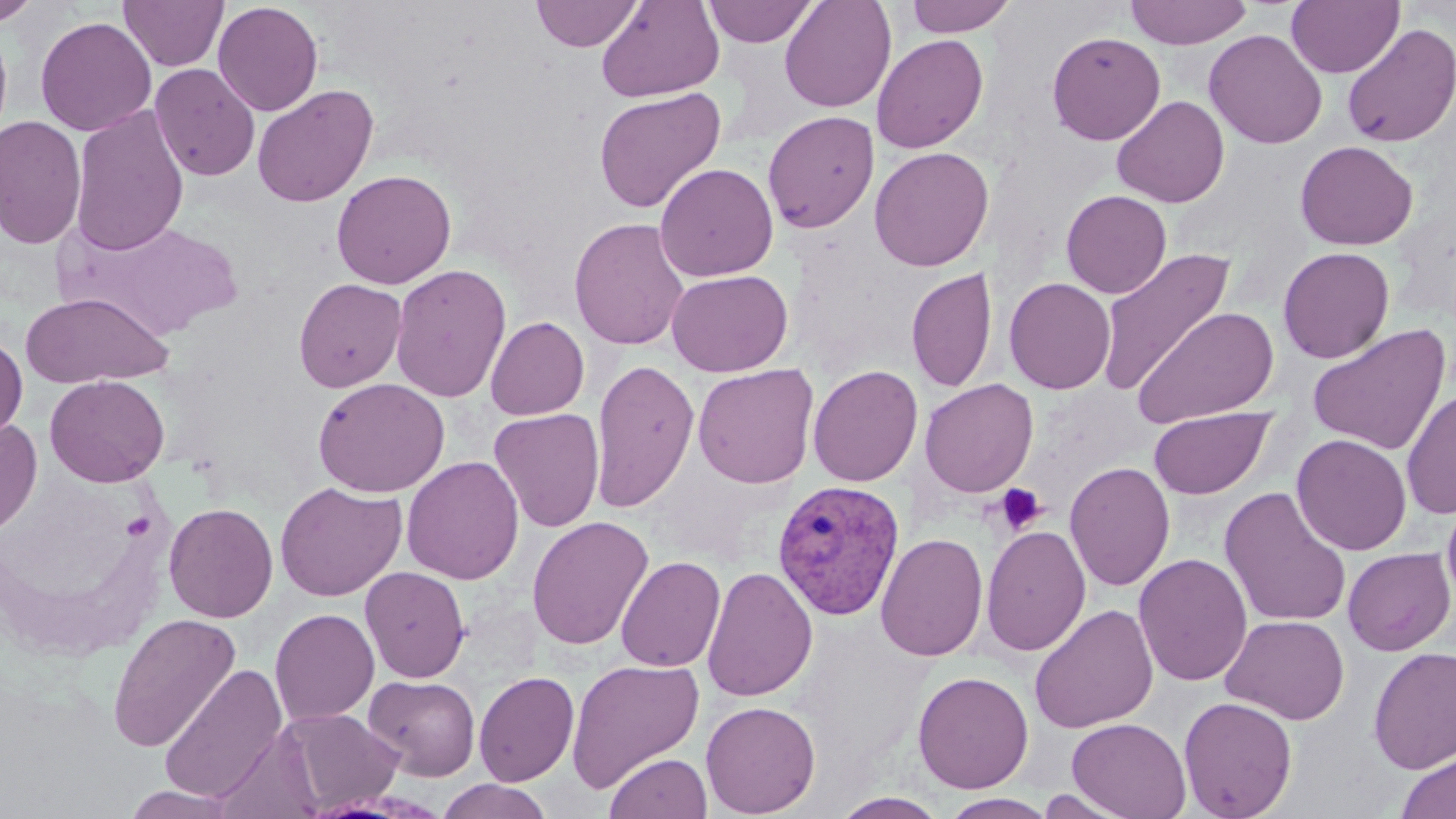
Summary:
  - Coordinate format: approximate bounding boxes as named x1/y1/x2/y2 corners in pixels
  - Uninfected red blood cell locations: (x1=0, y1=0, x2=42, y2=26), (x1=118, y1=0, x2=229, y2=71), (x1=530, y1=0, x2=644, y2=51), (x1=596, y1=0, x2=724, y2=102), (x1=703, y1=0, x2=818, y2=47), (x1=779, y1=0, x2=896, y2=113), (x1=904, y1=0, x2=1018, y2=37), (x1=1125, y1=0, x2=1253, y2=49), (x1=213, y1=1, x2=324, y2=116), (x1=1286, y1=1, x2=1404, y2=78), (x1=35, y1=16, x2=157, y2=136), (x1=1341, y1=24, x2=1456, y2=148), (x1=1204, y1=28, x2=1327, y2=149), (x1=1047, y1=30, x2=1166, y2=145), (x1=872, y1=34, x2=988, y2=153), (x1=149, y1=63, x2=260, y2=182), (x1=252, y1=84, x2=378, y2=207), (x1=593, y1=88, x2=726, y2=213), (x1=1112, y1=95, x2=1229, y2=207), (x1=69, y1=104, x2=190, y2=256), (x1=762, y1=110, x2=880, y2=233), (x1=0, y1=115, x2=87, y2=250), (x1=1294, y1=140, x2=1418, y2=251), (x1=869, y1=146, x2=993, y2=272), (x1=654, y1=162, x2=779, y2=282), (x1=331, y1=169, x2=456, y2=289), (x1=1061, y1=189, x2=1172, y2=298), (x1=569, y1=217, x2=690, y2=350), (x1=1095, y1=247, x2=1236, y2=395), (x1=1278, y1=247, x2=1394, y2=363), (x1=390, y1=263, x2=511, y2=403), (x1=907, y1=267, x2=997, y2=393), (x1=667, y1=269, x2=793, y2=376), (x1=1003, y1=277, x2=1116, y2=394), (x1=293, y1=278, x2=407, y2=392), (x1=20, y1=292, x2=172, y2=388), (x1=1132, y1=306, x2=1280, y2=428), (x1=485, y1=316, x2=589, y2=420), (x1=1307, y1=324, x2=1451, y2=454), (x1=0, y1=335, x2=28, y2=444), (x1=590, y1=358, x2=699, y2=513), (x1=692, y1=364, x2=819, y2=489), (x1=807, y1=364, x2=923, y2=487), (x1=45, y1=375, x2=169, y2=487), (x1=312, y1=377, x2=450, y2=497), (x1=919, y1=378, x2=1038, y2=497), (x1=1401, y1=388, x2=1456, y2=519), (x1=1148, y1=407, x2=1275, y2=499), (x1=488, y1=408, x2=605, y2=533), (x1=0, y1=417, x2=42, y2=536), (x1=1291, y1=433, x2=1412, y2=556), (x1=401, y1=456, x2=524, y2=584), (x1=1063, y1=461, x2=1176, y2=592), (x1=275, y1=481, x2=406, y2=601), (x1=1219, y1=486, x2=1352, y2=628), (x1=1441, y1=488, x2=1456, y2=611), (x1=163, y1=502, x2=279, y2=623), (x1=526, y1=516, x2=654, y2=651), (x1=981, y1=524, x2=1091, y2=656), (x1=875, y1=532, x2=988, y2=662), (x1=1342, y1=547, x2=1455, y2=655), (x1=1133, y1=553, x2=1252, y2=687), (x1=616, y1=555, x2=725, y2=673), (x1=701, y1=565, x2=818, y2=702), (x1=359, y1=566, x2=470, y2=683), (x1=1029, y1=603, x2=1158, y2=733), (x1=270, y1=608, x2=379, y2=726), (x1=106, y1=612, x2=241, y2=753), (x1=1220, y1=614, x2=1349, y2=725), (x1=1367, y1=646, x2=1456, y2=773), (x1=566, y1=658, x2=705, y2=792), (x1=158, y1=663, x2=287, y2=804), (x1=473, y1=670, x2=579, y2=786), (x1=912, y1=670, x2=1034, y2=793), (x1=364, y1=674, x2=480, y2=781), (x1=1178, y1=696, x2=1297, y2=819), (x1=700, y1=700, x2=821, y2=817), (x1=277, y1=707, x2=403, y2=812), (x1=1066, y1=717, x2=1191, y2=819), (x1=210, y1=727, x2=326, y2=819), (x1=1396, y1=750, x2=1456, y2=819), (x1=604, y1=751, x2=712, y2=819), (x1=436, y1=778, x2=554, y2=819), (x1=121, y1=786, x2=243, y2=819), (x1=1034, y1=788, x2=1136, y2=818), (x1=830, y1=791, x2=950, y2=818), (x1=939, y1=793, x2=1058, y2=819)
  - Plasmodium vivax-infected red blood cell locations: (x1=771, y1=479, x2=906, y2=621)
  - Platelet locations: (x1=994, y1=483, x2=1046, y2=533)
  - Slide-level diagnosis: Plasmodium vivax
  - Image size: 1456×819 pixels
  - Field of view: one of a larger specimen
  - Stain: May-Grünwald-Giemsa
  - Magnification: 1000x
  - Modality: light microscopy
  - Preparation: thin blood film